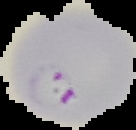

Malaria status: parasitized. From a thin blood film. Image is 136×130 pixels. The area outside the segmented cell region is set to black.